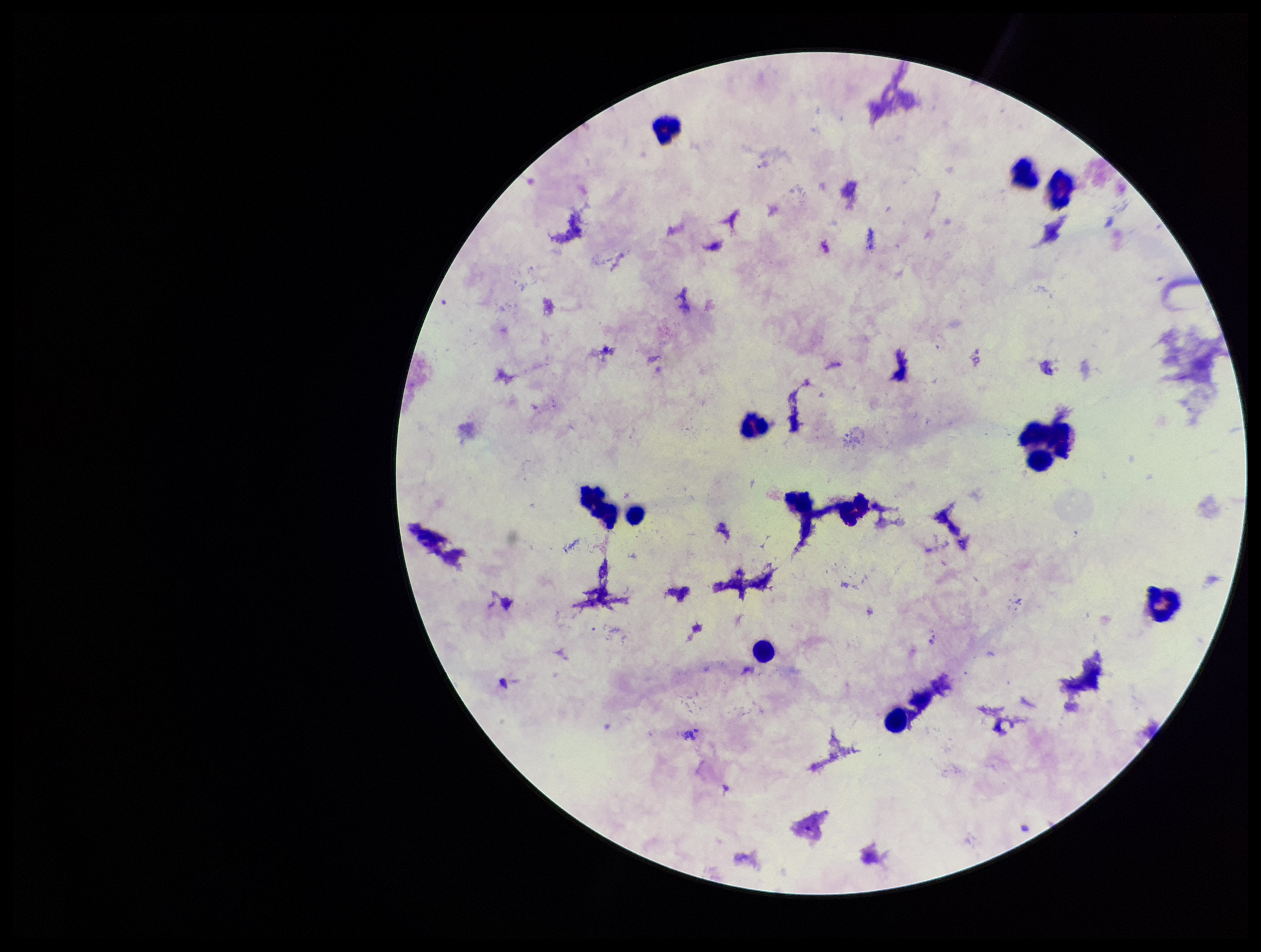

Image is 1261×952 pixels. Preparation: thick. Photographed through the microscope eyepiece with a smartphone camera. One field from this slide. Parasite count: 0. Stained with Giemsa. Plasmodium parasites: none seen. Patient malaria status: negative. Leukocyte count: 12.